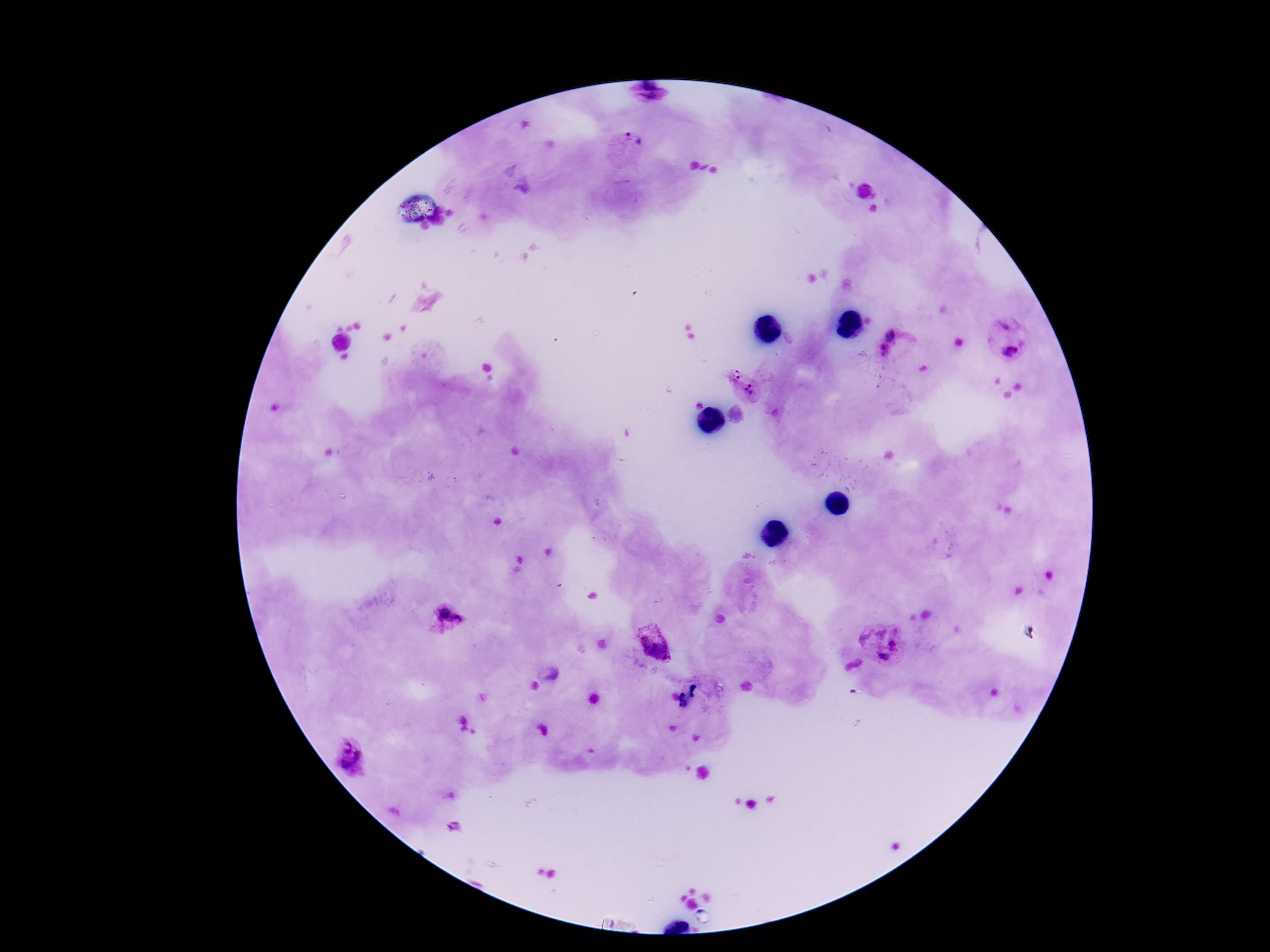 Approximate object centers, in pixels from the top-left corner. Plasmodium parasite locations: (x=649, y=94), (x=629, y=142), (x=1005, y=324), (x=893, y=335), (x=1010, y=351), (x=882, y=353), (x=735, y=375), (x=749, y=390), (x=449, y=616), (x=881, y=644), (x=654, y=646), (x=352, y=756), (x=454, y=827). Image is 1270×952 pixels. Patient malaria status: infected. Photographed through the microscope eyepiece with a smartphone camera. Giemsa-stained preparation. 100x magnification. One field from this slide. Thick blood smear.